Assess this cell for malaria.
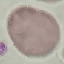
It is uninfected.

{
  "preparation": "thin blood smear",
  "image_type": "automatically extracted cell patch, resized to 64 × 64 pixels",
  "stain": "Giemsa",
  "capture": "smartphone camera at the microscope eyepiece"
}